Describe the morphology of the erythrocytes.
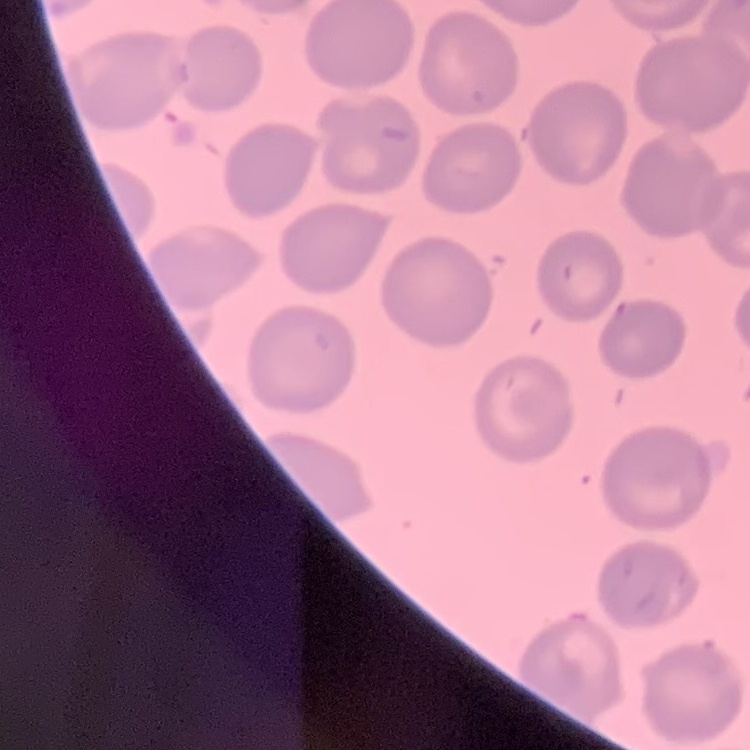
No rouleaux formation.

Square crop of a larger photomicrograph. Field's or Giemsa stain. Thin peripheral smear.